Give the preparation type.
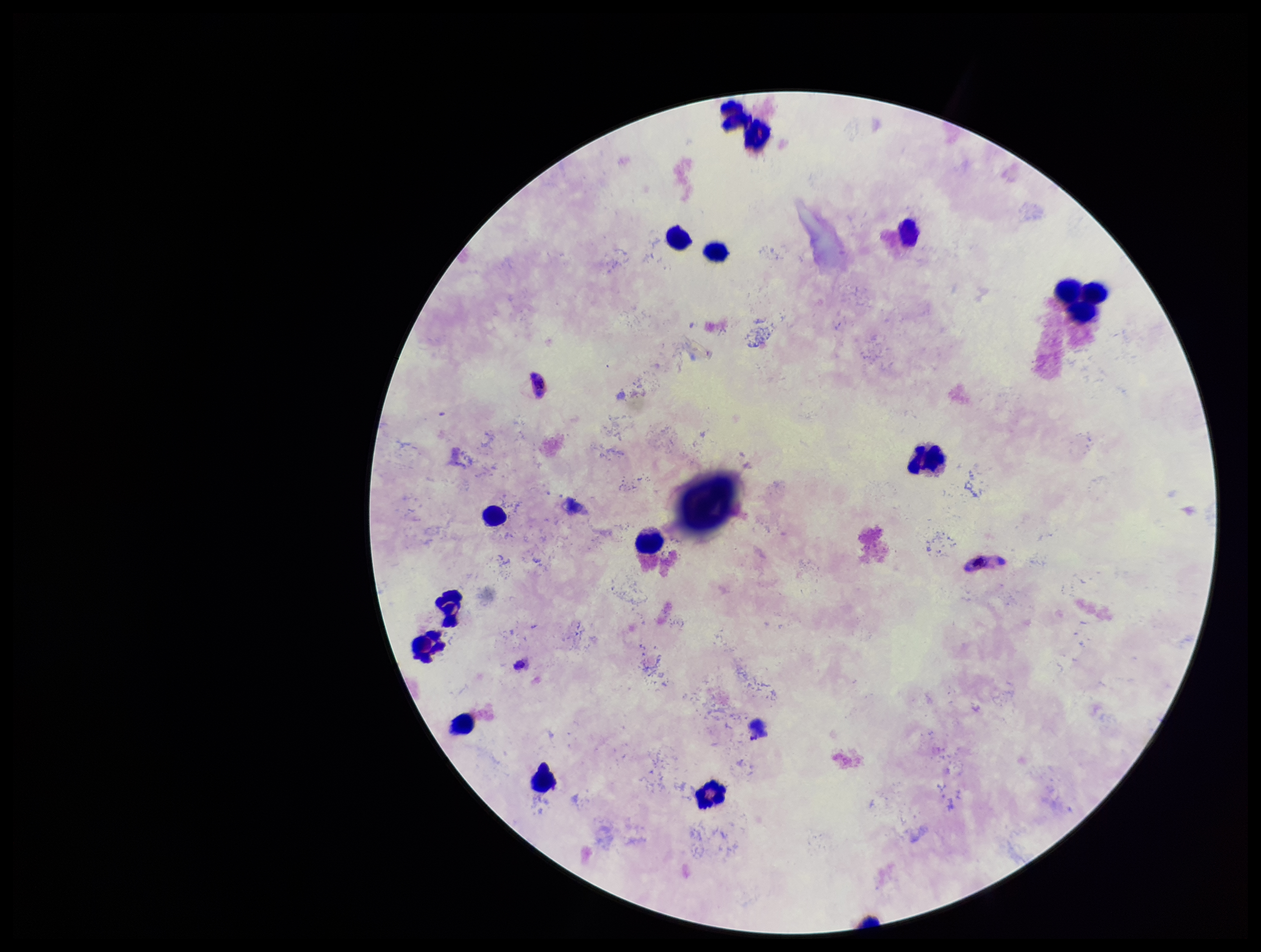
It is a thick blood smear.

Summary:
  - Capture: smartphone photograph through the microscope eyepiece
  - Leukocyte count: 15
  - Parasite count: 0
  - Species reported for this patient: Plasmodium falciparum
  - Plasmodium parasites: none detected
  - Field of view: one from this slide
  - Image size: 1261×952 pixels
  - Stain: Giemsa
  - Patient malaria status: positive